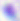
{
  "identification": "Toxoplasma gondii",
  "magnification": "400x",
  "modality": "photomicrograph"
}